Name the parasite shown.
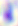
Toxoplasma gondii.

Summary:
  - Modality: micrograph
  - Magnification: 400x